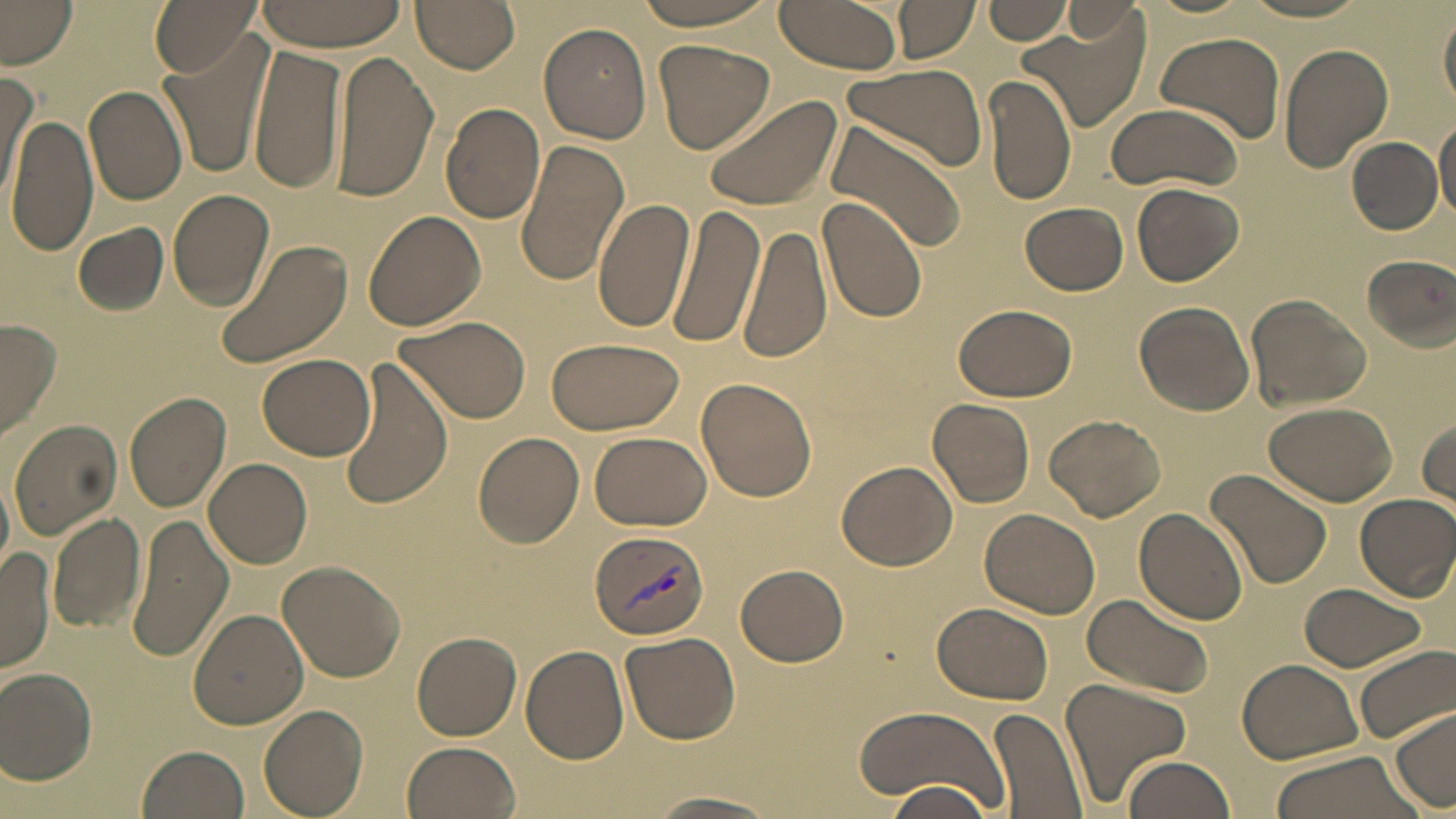
Summary:
  - Coordinate format: approximate bounding boxes as [x1, y1, x2, y2] in pixels
  - Uninfected red blood cell locations: [1, 0, 79, 68], [149, 0, 261, 76], [410, 0, 521, 73], [628, 0, 782, 32], [774, 0, 907, 74], [984, 0, 1073, 46], [250, 1, 410, 50], [895, 1, 978, 63], [1239, 1, 1373, 22], [1062, 3, 1146, 44], [1439, 8, 1456, 111], [1016, 19, 1147, 132], [539, 23, 653, 145], [1153, 31, 1286, 142], [158, 38, 269, 179], [654, 39, 775, 154], [247, 42, 348, 199], [1278, 43, 1393, 173], [331, 51, 440, 203], [840, 61, 991, 173], [0, 67, 36, 199], [984, 75, 1077, 206], [83, 85, 189, 206], [699, 95, 843, 214], [3, 99, 183, 237], [1104, 101, 1243, 193], [441, 102, 546, 225], [7, 112, 97, 257], [821, 116, 968, 254], [1434, 117, 1456, 222], [1346, 137, 1443, 235], [514, 138, 629, 288], [1134, 181, 1244, 287], [168, 188, 276, 311], [818, 194, 929, 325], [592, 197, 697, 333], [665, 202, 766, 352], [1021, 202, 1128, 295], [363, 210, 486, 332], [73, 222, 168, 315], [740, 222, 832, 366], [214, 238, 354, 369], [1360, 254, 1456, 351], [1244, 293, 1373, 410], [951, 300, 1080, 401], [1134, 302, 1255, 416], [394, 313, 532, 423], [1, 320, 60, 441], [545, 337, 686, 435], [257, 350, 376, 461], [335, 356, 454, 511], [696, 376, 818, 502], [124, 391, 232, 513], [927, 397, 1036, 509], [1264, 401, 1397, 506], [1044, 413, 1166, 522], [1415, 415, 1455, 509], [9, 419, 122, 540], [472, 430, 587, 549], [588, 430, 712, 530], [203, 457, 313, 570], [836, 461, 957, 571], [1205, 468, 1332, 590], [0, 471, 13, 585], [1354, 492, 1456, 601], [1135, 507, 1249, 624], [980, 508, 1101, 619], [48, 510, 146, 635], [124, 514, 234, 662], [1, 547, 54, 672], [276, 559, 406, 682], [737, 563, 849, 667], [1297, 582, 1428, 673], [1082, 592, 1214, 699], [932, 603, 1052, 705], [188, 608, 310, 730], [411, 631, 521, 741], [621, 631, 742, 745], [1352, 643, 1456, 745], [520, 645, 628, 765], [1238, 657, 1364, 763], [0, 666, 99, 783], [1058, 676, 1191, 805], [258, 704, 369, 818], [853, 705, 1014, 812], [991, 705, 1089, 819], [1390, 708, 1455, 812], [401, 741, 523, 819], [135, 745, 250, 819], [1267, 751, 1423, 819], [1118, 755, 1234, 819], [880, 781, 997, 814], [647, 790, 783, 817]
  - Plasmodium vivax-infected red blood cell locations: [587, 528, 711, 641]
  - Slide-level diagnosis: Plasmodium vivax
  - Image size: 1456×819 pixels
  - Field of view: single
  - Modality: light microscopy
  - Preparation: thin blood film
  - Stain: May-Grünwald-Giemsa
  - Magnification: 1000x